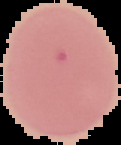 Malaria status: uninfected. The area outside the segmented cell region is set to black. Image is 121×145 pixels. From a thin blood smear.